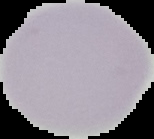
The area outside the segmented cell region is set to black. From a thin blood film. Result: no Plasmodium parasites detected. Image is 154×139 pixels.